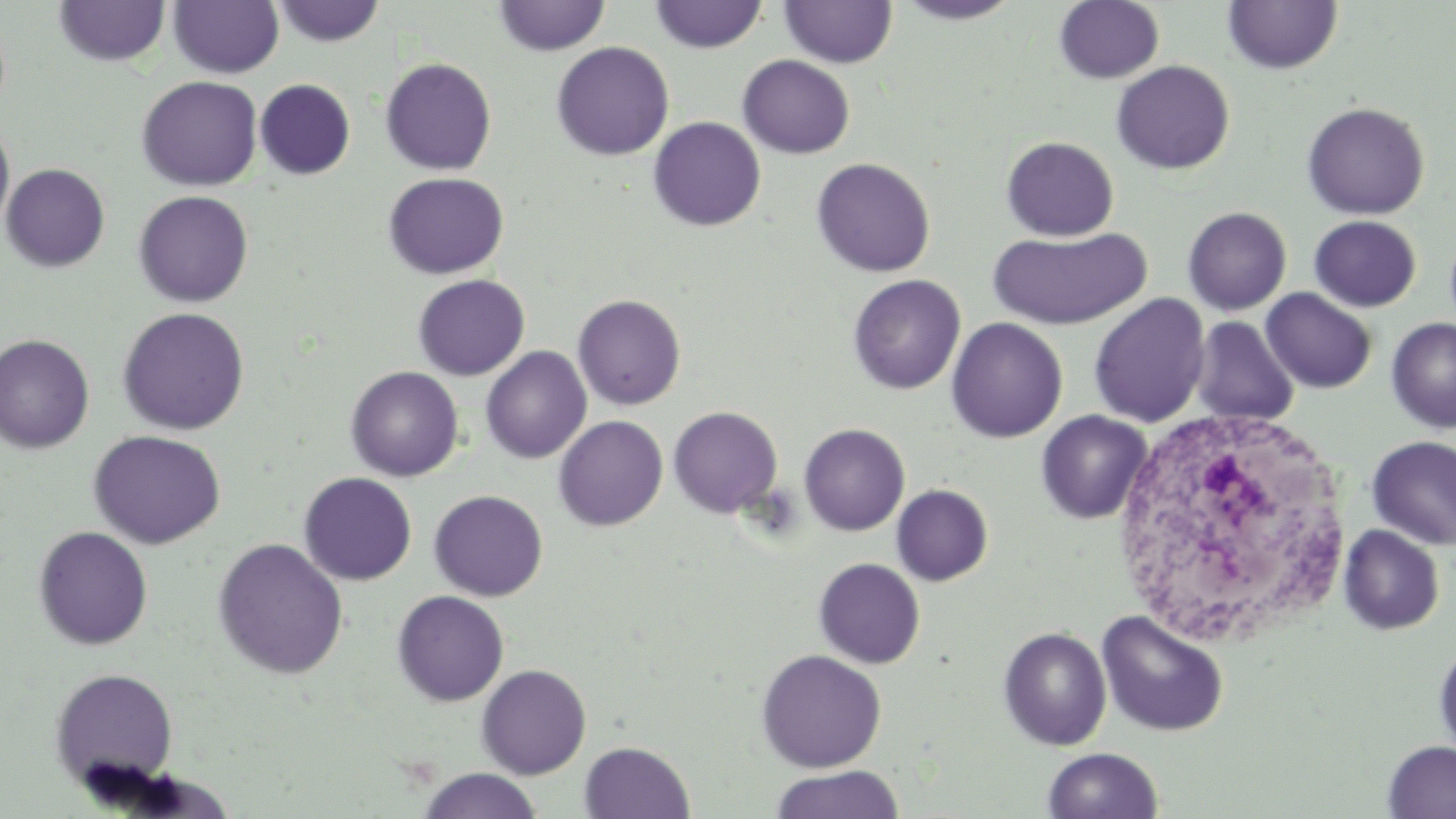
slide-level diagnosis = negative for blood parasites
image size = 1456×819 pixels
modality = optical microscopy
stain = May-Grünwald-Giemsa
preparation = thin blood film
white blood cell locations = approximate bounding boxes as named x1/y1/x2/y2 corners in pixels: (x1=1105, y1=410, x2=1351, y2=646)
uninfected red blood cell locations = approximate bounding boxes as named x1/y1/x2/y2 corners in pixels: (x1=779, y1=0, x2=897, y2=68), (x1=1054, y1=0, x2=1164, y2=84), (x1=1223, y1=0, x2=1343, y2=75), (x1=54, y1=1, x2=171, y2=66), (x1=169, y1=1, x2=284, y2=78), (x1=272, y1=1, x2=386, y2=47), (x1=493, y1=1, x2=611, y2=56), (x1=649, y1=1, x2=769, y2=53), (x1=894, y1=1, x2=1023, y2=25), (x1=551, y1=42, x2=674, y2=160), (x1=738, y1=54, x2=855, y2=158), (x1=379, y1=57, x2=497, y2=176), (x1=1111, y1=60, x2=1234, y2=175), (x1=136, y1=75, x2=262, y2=191), (x1=255, y1=79, x2=356, y2=180), (x1=1301, y1=101, x2=1430, y2=220), (x1=648, y1=116, x2=766, y2=232), (x1=0, y1=120, x2=15, y2=236), (x1=1001, y1=136, x2=1120, y2=241), (x1=811, y1=157, x2=935, y2=277), (x1=1, y1=163, x2=110, y2=272), (x1=383, y1=172, x2=508, y2=279), (x1=133, y1=190, x2=253, y2=308), (x1=1182, y1=206, x2=1292, y2=315), (x1=1308, y1=215, x2=1421, y2=312), (x1=988, y1=226, x2=1152, y2=330), (x1=412, y1=274, x2=530, y2=381), (x1=847, y1=274, x2=966, y2=395), (x1=1261, y1=288, x2=1376, y2=393), (x1=1088, y1=293, x2=1211, y2=427), (x1=573, y1=294, x2=686, y2=411), (x1=117, y1=307, x2=250, y2=435), (x1=1190, y1=316, x2=1300, y2=427), (x1=946, y1=317, x2=1068, y2=443), (x1=1386, y1=317, x2=1456, y2=433), (x1=0, y1=334, x2=95, y2=453), (x1=480, y1=346, x2=592, y2=464), (x1=345, y1=366, x2=464, y2=481), (x1=668, y1=405, x2=783, y2=517), (x1=1035, y1=410, x2=1153, y2=525), (x1=553, y1=415, x2=668, y2=531), (x1=798, y1=423, x2=910, y2=536), (x1=88, y1=430, x2=227, y2=549), (x1=1366, y1=436, x2=1456, y2=550), (x1=299, y1=472, x2=417, y2=585), (x1=891, y1=484, x2=993, y2=586), (x1=429, y1=490, x2=548, y2=601), (x1=1338, y1=525, x2=1445, y2=635), (x1=32, y1=526, x2=154, y2=650), (x1=212, y1=538, x2=349, y2=680), (x1=813, y1=558, x2=925, y2=669), (x1=392, y1=590, x2=509, y2=706), (x1=1096, y1=610, x2=1230, y2=738), (x1=997, y1=627, x2=1112, y2=750), (x1=1433, y1=640, x2=1456, y2=762), (x1=755, y1=649, x2=887, y2=773), (x1=476, y1=664, x2=592, y2=779), (x1=48, y1=667, x2=179, y2=793), (x1=579, y1=741, x2=695, y2=819), (x1=1382, y1=741, x2=1456, y2=819), (x1=1041, y1=747, x2=1164, y2=819), (x1=770, y1=765, x2=905, y2=818), (x1=416, y1=768, x2=544, y2=819)
magnification = 1000x
field of view = one of a larger specimen